Identify the parasite.
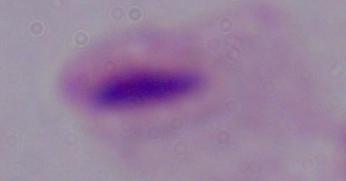
This is a trichomonad.

magnification = 1000x
modality = photomicrograph